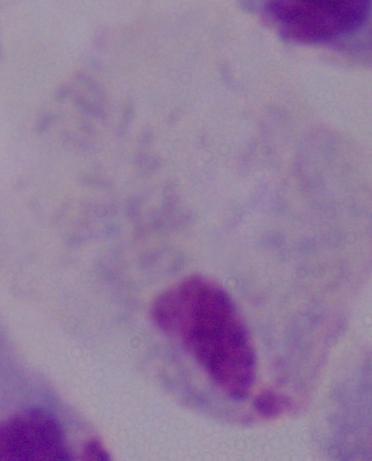
Photomicrograph. A trichomonad is shown. Captured at 1000x magnification.